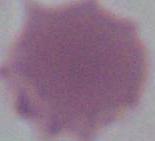
Summary:
  - Modality: photomicrograph
  - Magnification: 1000x
  - Identification: erythrocyte